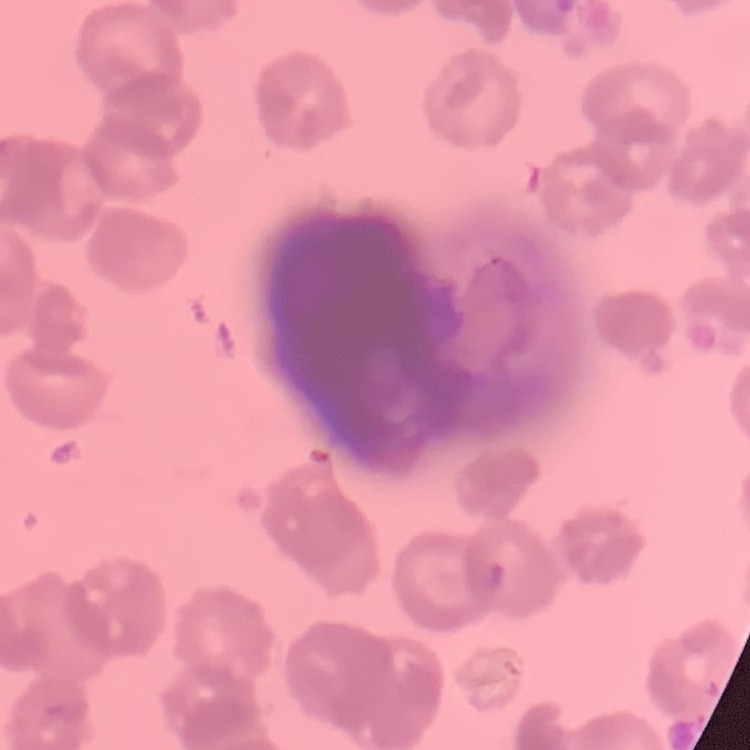

Summary:
  - Erythrocyte morphology: rouleaux formation
  - Preparation: thin peripheral smear
  - Stain: Field's or Giemsa
  - Image type: one tile cut from a larger photomicrograph